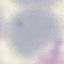

Summary:
  - Result: no malaria parasites seen
  - Capture: smartphone camera at the microscope eyepiece
  - Image type: cell patch, automatically extracted from a larger field of view and resized to 64 × 64 pixels
  - Preparation: thin blood smear
  - Stain: Giemsa